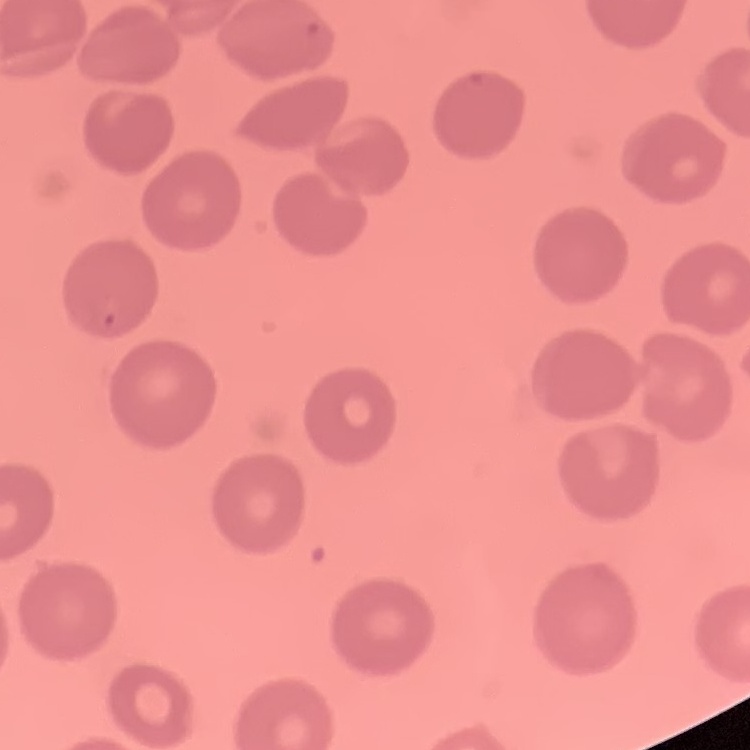

erythrocyte_morphology: no rouleaux formation
stain: Field's or Giemsa
preparation: thin blood smear
image_type: square crop of a larger photomicrograph